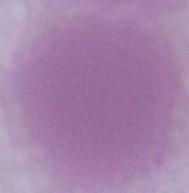
modality: micrograph
magnification: 1000x
identification: erythrocyte